Outline each blood parasite and name the species.
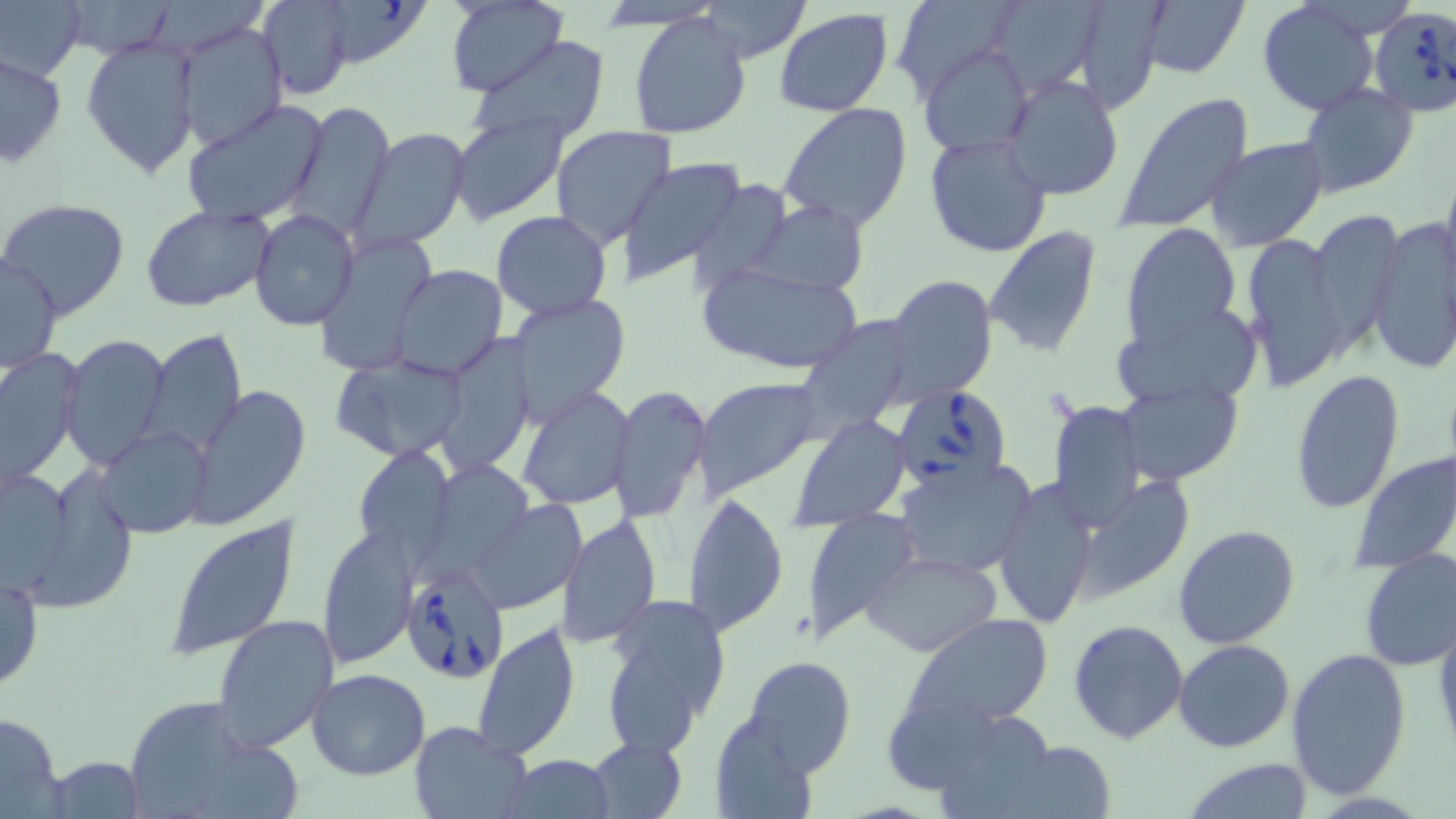

Approximate bounding boxes as named x1/y1/x2/y2 corners in pixels.
Babesia divergens-infected red blood cells: (x1=1369, y1=7, x2=1456, y2=120), (x1=896, y1=384, x2=1012, y2=492), (x1=400, y1=565, x2=511, y2=682).
No Plasmodium falciparum, Plasmodium ovale, Plasmodium malariae, Plasmodium vivax, or Trypanosoma brucei observed.

slide-level diagnosis = Babesia divergens
field of view = one of a larger specimen
uninfected red blood cell locations = approximate bounding boxes as named x1/y1/x2/y2 corners in pixels: (x1=60, y1=0, x2=181, y2=60), (x1=259, y1=0, x2=355, y2=99), (x1=315, y1=0, x2=434, y2=68), (x1=898, y1=0, x2=1011, y2=101), (x1=1071, y1=0, x2=1166, y2=112), (x1=1256, y1=0, x2=1383, y2=115), (x1=1, y1=1, x2=83, y2=81), (x1=445, y1=1, x2=567, y2=98), (x1=1002, y1=1, x2=1104, y2=91), (x1=1135, y1=1, x2=1250, y2=80), (x1=702, y1=2, x2=811, y2=62), (x1=627, y1=10, x2=753, y2=141), (x1=773, y1=10, x2=893, y2=117), (x1=173, y1=23, x2=287, y2=151), (x1=81, y1=34, x2=201, y2=181), (x1=469, y1=38, x2=612, y2=147), (x1=920, y1=41, x2=1034, y2=155), (x1=1, y1=52, x2=67, y2=166), (x1=1001, y1=74, x2=1124, y2=201), (x1=1297, y1=84, x2=1419, y2=198), (x1=1113, y1=93, x2=1255, y2=235), (x1=181, y1=98, x2=332, y2=226), (x1=287, y1=101, x2=394, y2=238), (x1=778, y1=103, x2=915, y2=232), (x1=448, y1=112, x2=567, y2=225), (x1=549, y1=125, x2=674, y2=248), (x1=352, y1=128, x2=470, y2=249), (x1=923, y1=134, x2=1052, y2=258), (x1=1205, y1=138, x2=1328, y2=251), (x1=617, y1=158, x2=748, y2=286), (x1=1439, y1=165, x2=1456, y2=287), (x1=687, y1=178, x2=790, y2=296), (x1=1, y1=198, x2=131, y2=319), (x1=750, y1=199, x2=870, y2=294), (x1=140, y1=204, x2=275, y2=312), (x1=248, y1=210, x2=360, y2=330), (x1=491, y1=211, x2=613, y2=320), (x1=1308, y1=212, x2=1404, y2=344), (x1=1365, y1=216, x2=1456, y2=374), (x1=1122, y1=223, x2=1241, y2=349), (x1=984, y1=226, x2=1102, y2=358), (x1=1242, y1=232, x2=1351, y2=387), (x1=315, y1=234, x2=442, y2=368), (x1=1, y1=252, x2=63, y2=376), (x1=697, y1=262, x2=864, y2=376), (x1=390, y1=264, x2=509, y2=379), (x1=887, y1=275, x2=999, y2=405), (x1=506, y1=290, x2=630, y2=422), (x1=796, y1=308, x2=907, y2=447), (x1=1115, y1=324, x2=1261, y2=408), (x1=140, y1=329, x2=247, y2=458), (x1=60, y1=334, x2=173, y2=471), (x1=436, y1=334, x2=536, y2=476), (x1=0, y1=347, x2=83, y2=490), (x1=332, y1=353, x2=469, y2=463), (x1=1291, y1=367, x2=1404, y2=514), (x1=692, y1=376, x2=824, y2=501), (x1=1118, y1=380, x2=1243, y2=486), (x1=184, y1=384, x2=310, y2=528), (x1=518, y1=385, x2=635, y2=512), (x1=611, y1=385, x2=712, y2=525), (x1=1049, y1=397, x2=1144, y2=530), (x1=790, y1=415, x2=911, y2=530), (x1=96, y1=425, x2=214, y2=538), (x1=354, y1=446, x2=456, y2=567), (x1=1350, y1=451, x2=1456, y2=574), (x1=894, y1=460, x2=1035, y2=580), (x1=17, y1=463, x2=139, y2=615), (x1=1, y1=466, x2=75, y2=594), (x1=1069, y1=474, x2=1197, y2=604), (x1=993, y1=476, x2=1098, y2=631), (x1=684, y1=490, x2=789, y2=637), (x1=467, y1=499, x2=589, y2=611), (x1=798, y1=510, x2=921, y2=645), (x1=557, y1=513, x2=660, y2=652), (x1=163, y1=516, x2=302, y2=661), (x1=1172, y1=524, x2=1300, y2=649), (x1=315, y1=529, x2=416, y2=669), (x1=863, y1=550, x2=1003, y2=656), (x1=1356, y1=550, x2=1456, y2=670), (x1=1, y1=568, x2=44, y2=697), (x1=601, y1=594, x2=733, y2=754), (x1=211, y1=613, x2=339, y2=753), (x1=901, y1=613, x2=1056, y2=732), (x1=1432, y1=617, x2=1456, y2=759), (x1=470, y1=619, x2=580, y2=762), (x1=1067, y1=619, x2=1189, y2=745), (x1=1172, y1=640, x2=1294, y2=754), (x1=1284, y1=645, x2=1413, y2=800), (x1=739, y1=654, x2=858, y2=775), (x1=309, y1=668, x2=430, y2=780), (x1=116, y1=700, x2=242, y2=818), (x1=888, y1=700, x2=1000, y2=790), (x1=0, y1=711, x2=66, y2=818), (x1=709, y1=711, x2=821, y2=817), (x1=941, y1=716, x2=1053, y2=819), (x1=408, y1=720, x2=532, y2=819), (x1=991, y1=735, x2=1119, y2=818), (x1=587, y1=736, x2=687, y2=817), (x1=200, y1=745, x2=300, y2=814), (x1=505, y1=755, x2=616, y2=818), (x1=56, y1=758, x2=144, y2=819), (x1=1181, y1=759, x2=1318, y2=817)
stain = May-Grünwald-Giemsa
image size = 1456×819 pixels
magnification = 1000x
modality = light microscopy
preparation = thin blood film